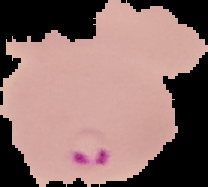
image_type: cell region segmented out of the field of view; surrounding area masked to black
preparation: thin blood film
image_size: 208×187 pixels
result: malaria parasites detected